Give the position of every Plasmodium parasite visible.
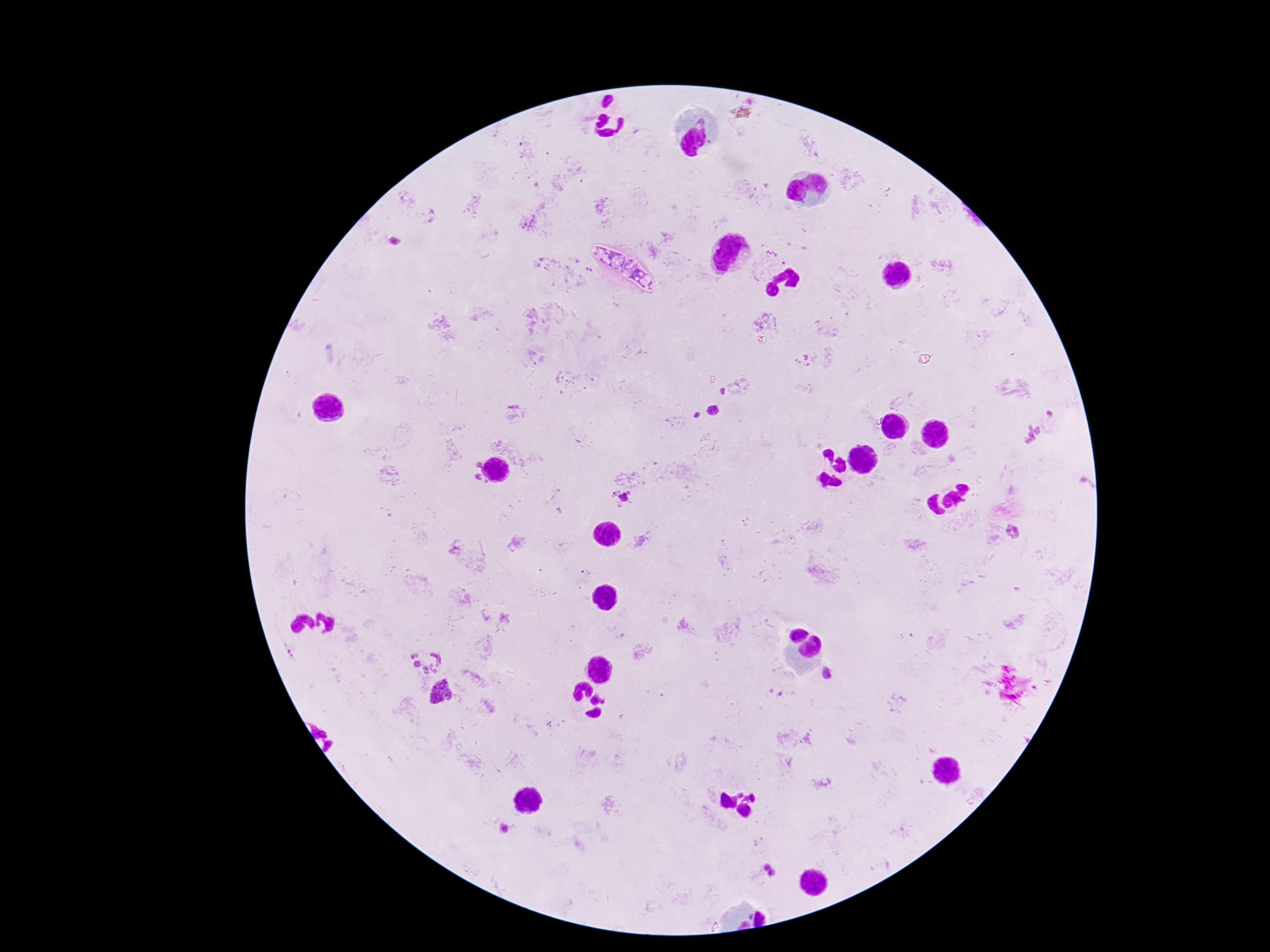

Approximate object centers, in pixels from the top-left corner.
Plasmodium parasites: (x=395, y=240), (x=806, y=357), (x=723, y=391), (x=712, y=409), (x=1050, y=413), (x=698, y=415), (x=1031, y=433), (x=479, y=464), (x=478, y=476), (x=629, y=491), (x=615, y=492), (x=623, y=497), (x=1013, y=532), (x=291, y=654), (x=414, y=654), (x=436, y=656), (x=417, y=664), (x=434, y=667), (x=425, y=671), (x=827, y=673), (x=443, y=691), (x=504, y=830), (x=766, y=866), (x=773, y=873).

Summary:
  - Patient malaria status: infected
  - Field of view: single
  - Stain: Giemsa
  - Preparation: thick peripheral-blood smear
  - Capture: smartphone camera through the microscope eyepiece
  - Image size: 1270×952 pixels
  - Magnification: 100x